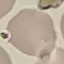
Summary:
  - Malaria status: uninfected
  - Stain: Giemsa
  - Preparation: thin blood film
  - Capture: smartphone camera at the microscope eyepiece
  - Image type: automatically extracted cell patch, resized to 64 × 64 pixels